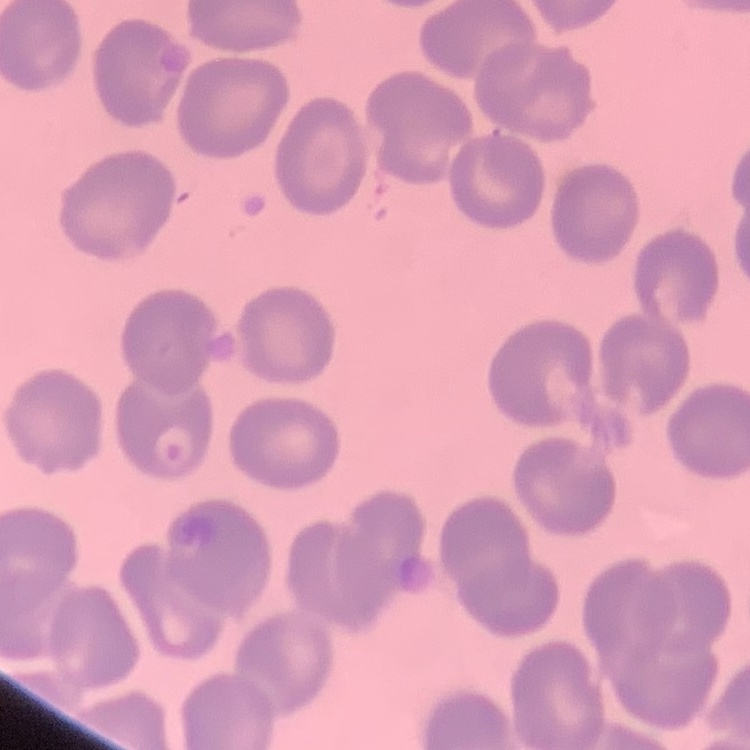 The red blood cells exhibit no rouleaux formation. One tile cut from a larger photomicrograph. Field's or Giemsa stain. Thin blood film.